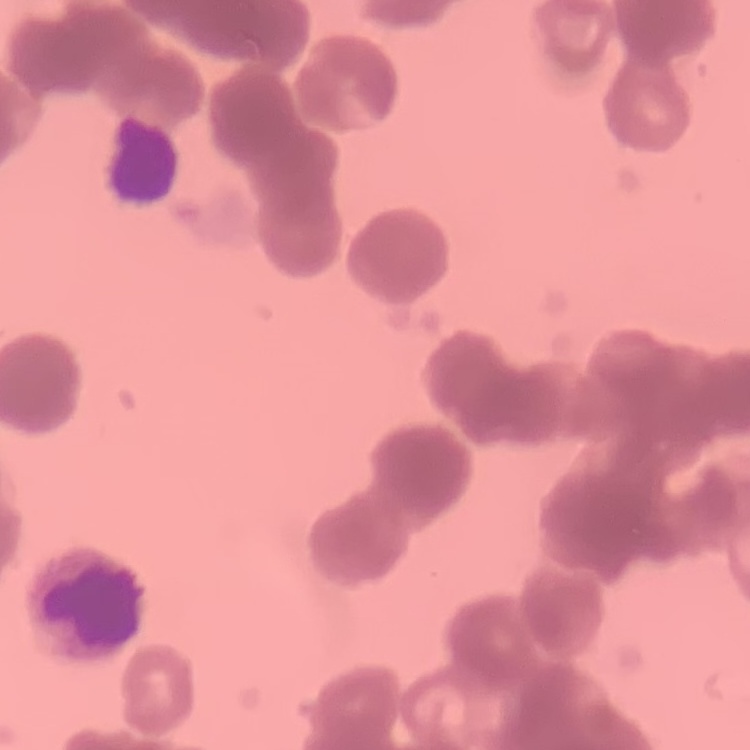
Summary:
  - Red blood cell morphology: rouleaux formation
  - Preparation: thin blood film
  - Image type: square crop of a larger photomicrograph
  - Stain: Field's or Giemsa